State which parasite is depicted.
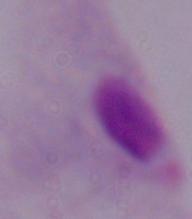
This is a trichomonad.

1000x magnification. Micrograph.